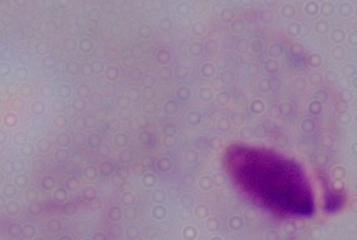
Summary:
  - Magnification: 1000x
  - Modality: micrograph
  - Identification: trichomonad